Describe the morphology of the erythrocytes.
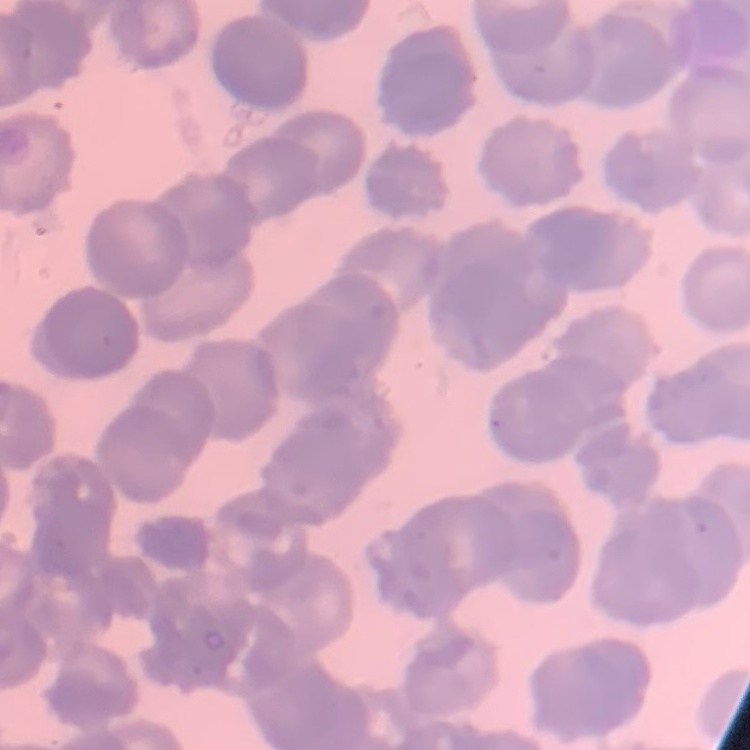

They show rouleaux formation.

image type = square crop of a larger photomicrograph
stain = Field's or Giemsa
preparation = thin blood smear